Give the position of every malaria parasite.
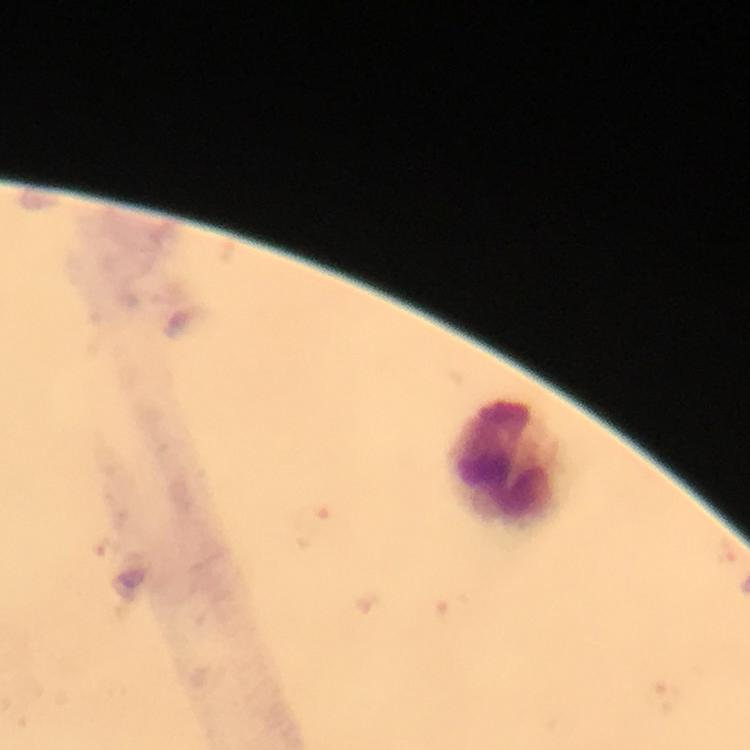

Approximate centers as (x, y) in pixels.
Malaria parasites: (314, 520), (108, 547).

cropped from = one field of view
immersion oil = used
preparation = thick smear
context = from a diagnostic examination for malaria
capture = smartphone photograph through a microscope
image size = 750×750 pixels
stain = Giemsa
leukocyte locations = approximate centers as (x, y) in pixels: (506, 464)
magnification = 100x